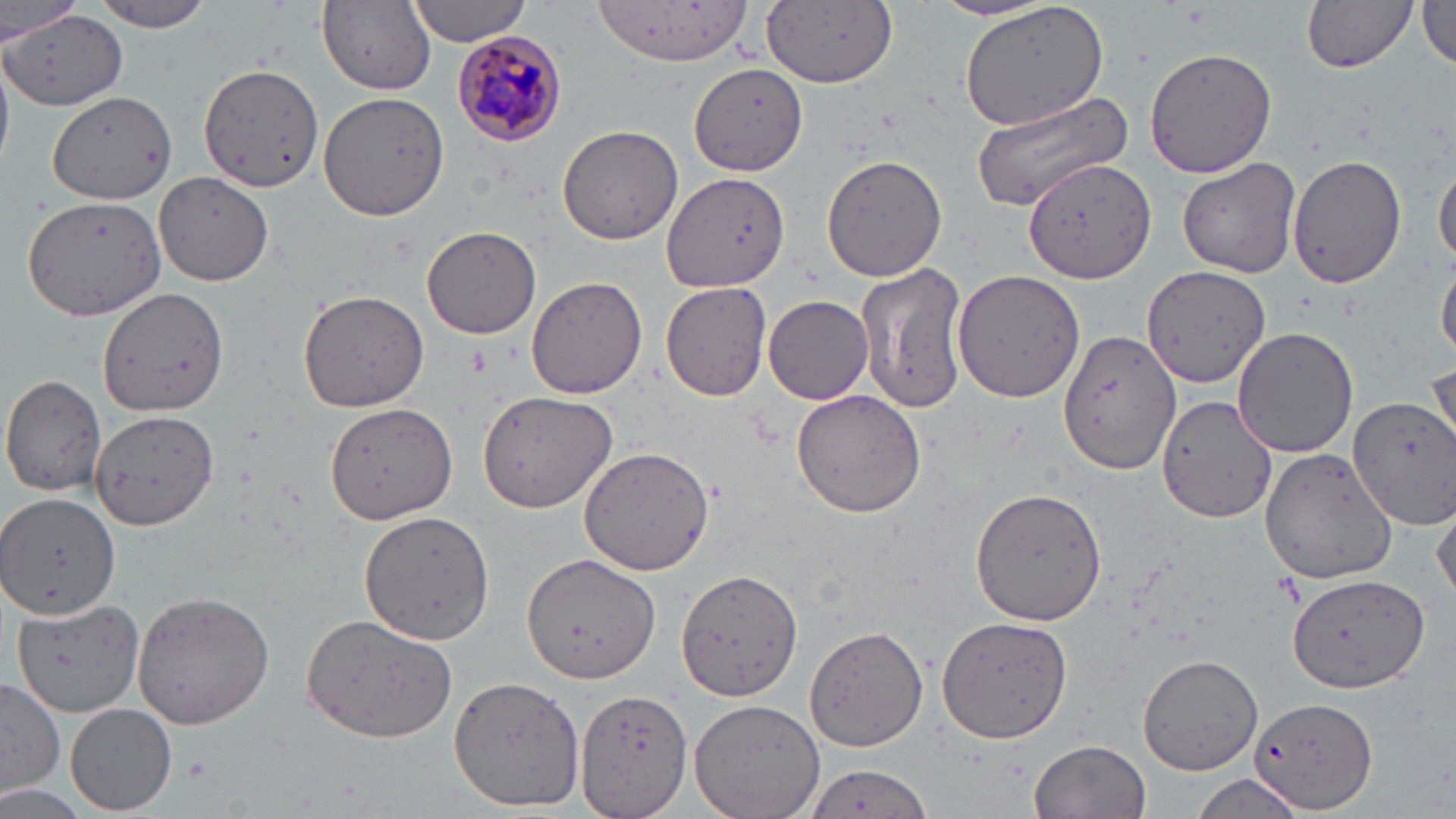

Summary:
  - Coordinate format: approximate bounding boxes as named x1/y1/x2/y2 corners in pixels
  - Plasmodium malariae-infected red blood cell locations: (x1=448, y1=29, x2=565, y2=148)
  - Uninfected red blood cell locations: (x1=89, y1=0, x2=218, y2=34), (x1=931, y1=0, x2=1062, y2=24), (x1=1300, y1=0, x2=1419, y2=73), (x1=1, y1=1, x2=81, y2=43), (x1=404, y1=1, x2=534, y2=47), (x1=595, y1=1, x2=754, y2=66), (x1=760, y1=2, x2=897, y2=89), (x1=957, y1=2, x2=1109, y2=132), (x1=317, y1=3, x2=438, y2=95), (x1=1417, y1=3, x2=1456, y2=72), (x1=2, y1=11, x2=127, y2=112), (x1=1145, y1=46, x2=1279, y2=178), (x1=0, y1=48, x2=14, y2=171), (x1=198, y1=62, x2=324, y2=191), (x1=690, y1=65, x2=807, y2=172), (x1=47, y1=90, x2=175, y2=205), (x1=319, y1=91, x2=449, y2=221), (x1=968, y1=94, x2=1136, y2=211), (x1=557, y1=125, x2=685, y2=245), (x1=1285, y1=153, x2=1406, y2=288), (x1=821, y1=154, x2=948, y2=281), (x1=1022, y1=157, x2=1156, y2=284), (x1=1178, y1=157, x2=1301, y2=279), (x1=1434, y1=158, x2=1456, y2=272), (x1=662, y1=172, x2=789, y2=293), (x1=153, y1=173, x2=274, y2=285), (x1=21, y1=192, x2=167, y2=322), (x1=421, y1=225, x2=541, y2=339), (x1=1438, y1=260, x2=1456, y2=359), (x1=859, y1=264, x2=971, y2=414), (x1=1143, y1=265, x2=1274, y2=392), (x1=951, y1=269, x2=1084, y2=402), (x1=526, y1=277, x2=647, y2=399), (x1=661, y1=281, x2=773, y2=402), (x1=297, y1=288, x2=429, y2=413), (x1=95, y1=289, x2=226, y2=416), (x1=763, y1=294, x2=875, y2=404), (x1=1232, y1=325, x2=1359, y2=459), (x1=1057, y1=329, x2=1181, y2=475), (x1=1429, y1=363, x2=1456, y2=456), (x1=0, y1=374, x2=110, y2=497), (x1=477, y1=388, x2=620, y2=514), (x1=791, y1=390, x2=926, y2=517), (x1=1158, y1=391, x2=1275, y2=523), (x1=1156, y1=394, x2=1277, y2=524), (x1=1351, y1=396, x2=1456, y2=532), (x1=325, y1=405, x2=457, y2=524), (x1=92, y1=409, x2=220, y2=532), (x1=578, y1=446, x2=714, y2=575), (x1=1258, y1=446, x2=1398, y2=583), (x1=970, y1=487, x2=1107, y2=626), (x1=0, y1=492, x2=120, y2=619), (x1=1432, y1=495, x2=1456, y2=605), (x1=359, y1=509, x2=494, y2=647), (x1=524, y1=552, x2=662, y2=682), (x1=678, y1=571, x2=803, y2=700), (x1=1283, y1=574, x2=1429, y2=695), (x1=130, y1=591, x2=275, y2=728), (x1=10, y1=598, x2=144, y2=718), (x1=301, y1=612, x2=458, y2=742), (x1=938, y1=614, x2=1072, y2=745), (x1=805, y1=624, x2=930, y2=753), (x1=1138, y1=653, x2=1264, y2=776), (x1=1, y1=676, x2=63, y2=799), (x1=450, y1=676, x2=585, y2=811), (x1=573, y1=688, x2=693, y2=818), (x1=1248, y1=696, x2=1377, y2=815), (x1=690, y1=697, x2=826, y2=819), (x1=66, y1=704, x2=177, y2=815), (x1=1029, y1=740, x2=1152, y2=819), (x1=799, y1=766, x2=936, y2=819), (x1=1190, y1=772, x2=1310, y2=819)
  - Slide-level diagnosis: Plasmodium malariae
  - Field of view: one of a larger specimen
  - Image size: 1456×819 pixels
  - Stain: May-Grünwald-Giemsa
  - Modality: light microscopy
  - Preparation: thin blood film
  - Magnification: 1000x